Locate every Plasmodium falciparum-infected red blood cell.
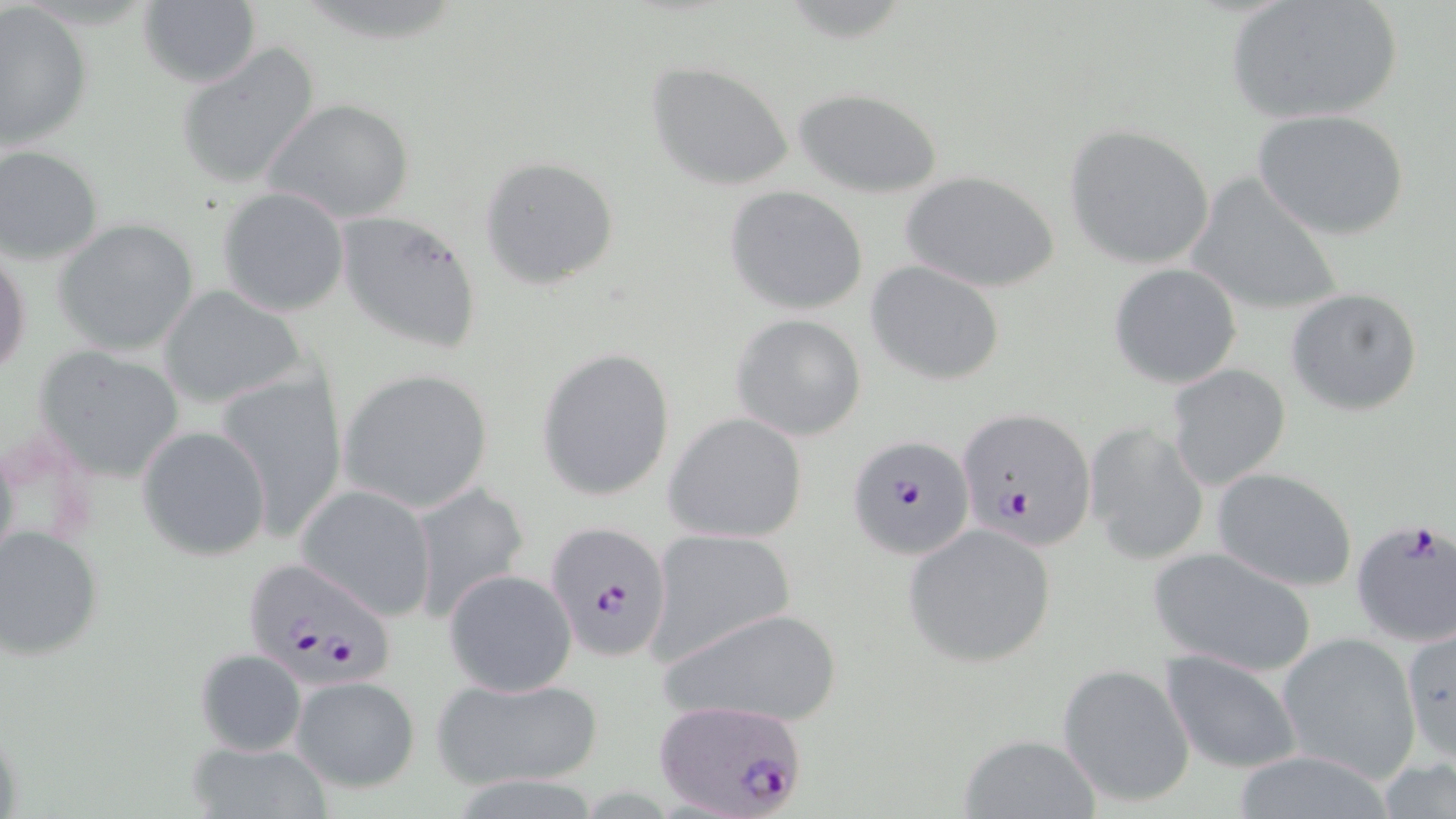
Approximate bounding boxes as (x1,y1)-(x2,y2) corner pairs in pixels.
Plasmodium falciparum-infected red blood cells: (956,408)-(1095,549), (847,433)-(977,562), (1350,517)-(1456,646), (543,520)-(673,663), (239,559)-(398,688), (651,701)-(810,819).

Uninfected red blood cell locations: (1225,0)-(1405,126), (137,2)-(262,87), (1,4)-(93,154), (175,41)-(323,191), (646,61)-(796,191), (793,88)-(943,198), (265,97)-(416,225), (1254,109)-(1410,240), (1063,124)-(1216,271), (0,143)-(106,266), (479,155)-(620,289), (899,169)-(1062,293), (1185,173)-(1346,320), (725,185)-(870,316), (217,186)-(349,316), (335,211)-(483,356), (54,218)-(199,356), (0,241)-(32,384), (866,261)-(1005,386), (1107,262)-(1243,389), (157,285)-(307,411), (1285,287)-(1424,415), (729,313)-(868,440), (34,345)-(187,483), (536,348)-(675,501), (1167,363)-(1292,492), (337,368)-(495,514), (215,369)-(350,537), (664,411)-(809,542), (1086,422)-(1210,566), (138,424)-(273,561), (1210,467)-(1359,592), (409,480)-(531,625), (295,482)-(438,622), (902,525)-(1058,668), (0,527)-(104,660), (647,528)-(796,667), (1147,546)-(1321,678), (444,569)-(578,697), (659,605)-(846,730), (1401,625)-(1454,765), (1277,631)-(1421,781), (194,648)-(307,757), (1159,649)-(1304,773), (1058,663)-(1196,809), (431,672)-(603,791), (290,675)-(420,792), (0,720)-(24,819), (957,732)-(1101,818), (189,740)-(332,817). Slide-level diagnosis: Plasmodium falciparum. One field of a larger specimen. Light microscopy. May-Grünwald-Giemsa-stained preparation. 1000x magnification. Thin blood smear. Image is 1456×819 pixels.